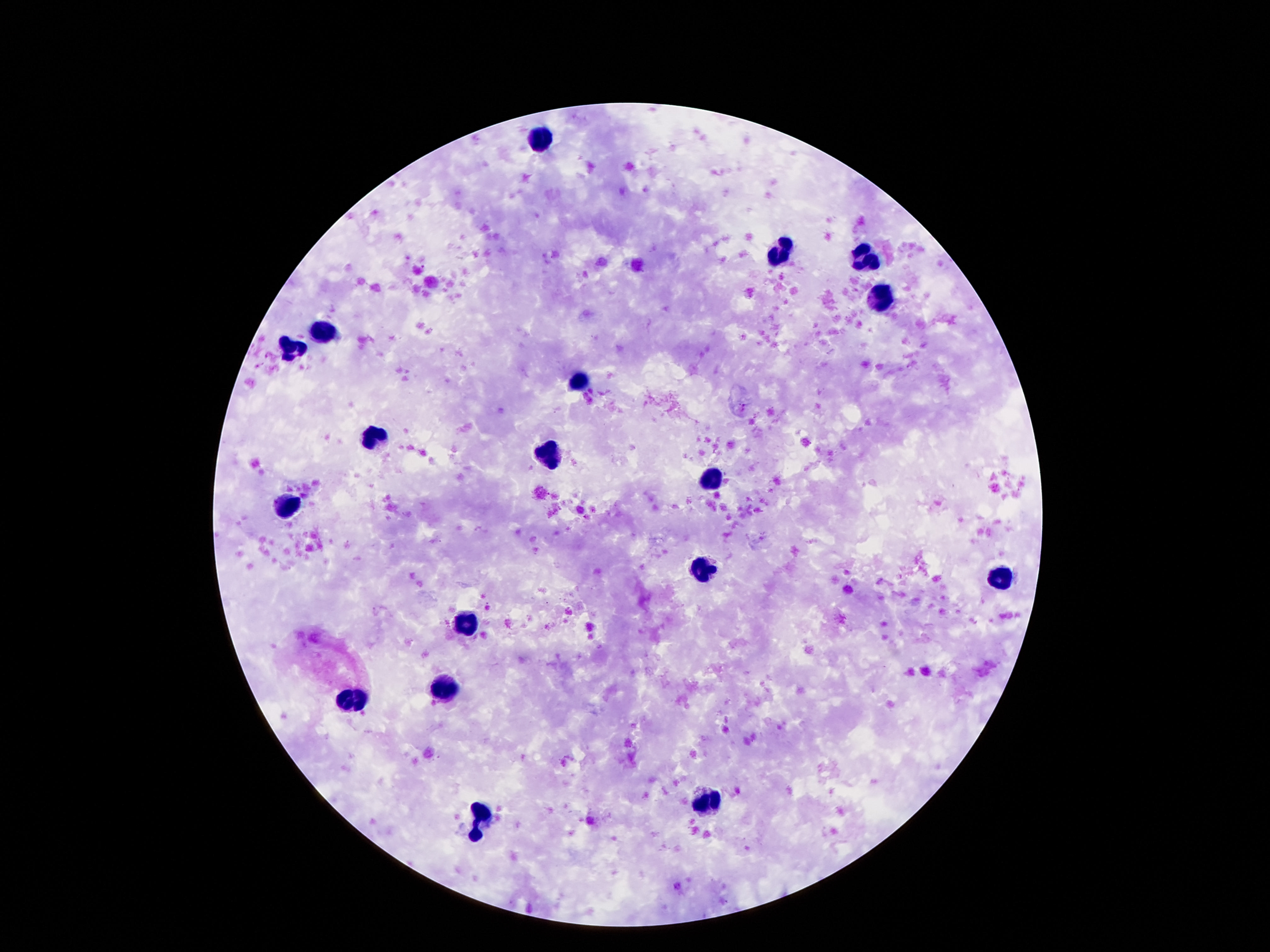
Approximate centers as [x, y] in pixels.
Summary:
  - Leukocyte locations: [544, 141], [781, 254], [866, 260], [882, 294], [330, 331], [290, 353], [574, 381], [374, 436], [549, 451], [712, 478], [292, 505], [702, 571], [998, 577], [463, 621], [446, 686], [355, 699], [710, 802], [477, 821]
  - Field of view: one from this slide
  - Stain: Giemsa
  - Patient malaria status: uninfected
  - Capture: smartphone camera through the microscope eyepiece
  - Magnification: 100x
  - Preparation: thick peripheral-blood smear
  - Image size: 1270×952 pixels